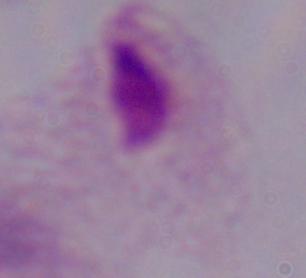
modality = photomicrograph
magnification = 1000x
identification = trichomonad